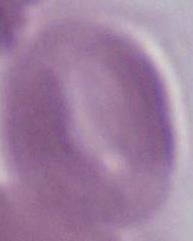
magnification = 1000x
identification = erythrocyte
modality = photomicrograph